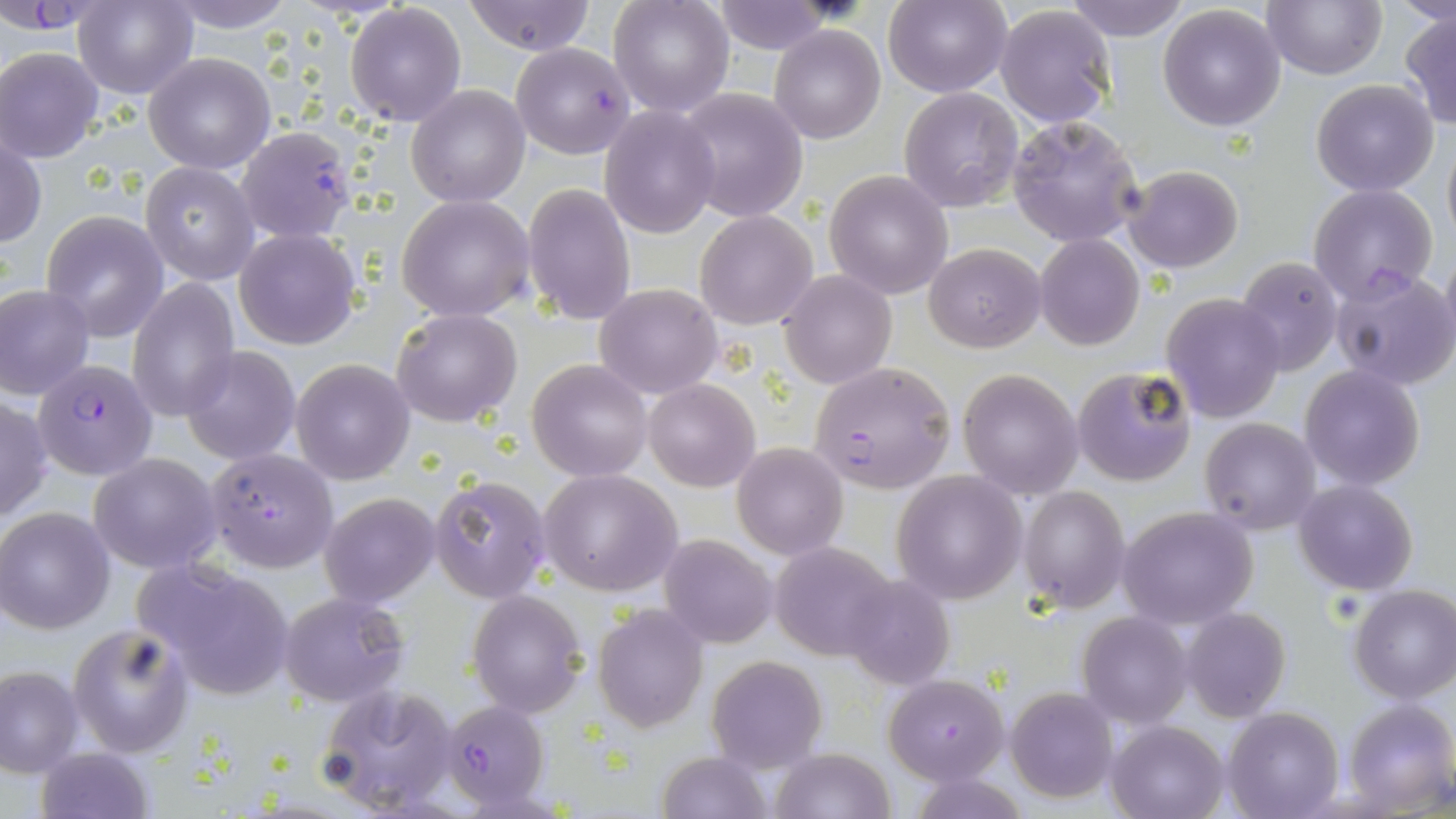

Approximate bounding boxes as [x1, y1, x2, y2] in pixels. Uninfected red blood cell locations: [165, 0, 293, 33], [462, 0, 597, 55], [607, 0, 734, 119], [884, 0, 1010, 97], [1063, 0, 1190, 42], [1263, 0, 1384, 80], [1392, 0, 1456, 31], [73, 1, 197, 101], [710, 2, 840, 53], [345, 3, 467, 127], [1157, 4, 1287, 131], [993, 5, 1116, 127], [1400, 11, 1456, 129], [770, 24, 887, 145], [0, 47, 104, 162], [143, 52, 276, 173], [1311, 79, 1440, 197], [406, 84, 530, 207], [898, 87, 1024, 213], [677, 88, 807, 221], [599, 105, 720, 238], [1008, 117, 1143, 247], [235, 126, 357, 242], [1, 136, 46, 249], [1442, 136, 1456, 248], [140, 162, 259, 283], [1123, 165, 1243, 273], [824, 169, 952, 299], [521, 182, 636, 326], [1309, 183, 1439, 302], [395, 193, 538, 322], [695, 210, 817, 330], [41, 212, 169, 340], [233, 227, 361, 350], [1034, 234, 1144, 351], [925, 242, 1046, 351], [1440, 244, 1456, 361], [1235, 256, 1343, 376], [1330, 265, 1455, 391], [778, 270, 896, 389], [128, 278, 240, 420], [595, 283, 724, 398], [0, 285, 95, 398], [1160, 293, 1286, 423], [392, 309, 521, 426], [181, 347, 301, 465], [527, 359, 653, 481], [291, 360, 414, 484], [1301, 365, 1424, 490], [1071, 366, 1198, 487], [958, 368, 1084, 498], [644, 378, 759, 490], [1, 392, 51, 525], [1201, 418, 1320, 535], [732, 441, 849, 560], [88, 452, 221, 575], [539, 468, 684, 596], [892, 468, 1026, 604], [432, 475, 550, 603], [1292, 479, 1418, 594], [1020, 485, 1131, 612], [319, 492, 440, 607], [1118, 506, 1260, 629], [1, 507, 116, 633], [661, 534, 779, 648], [769, 543, 894, 658], [131, 557, 298, 699], [842, 574, 958, 690], [1348, 585, 1456, 704], [468, 589, 588, 717], [279, 591, 408, 706], [593, 606, 709, 732], [1183, 609, 1292, 721], [1077, 612, 1192, 728], [68, 621, 197, 758], [706, 654, 828, 773], [0, 663, 82, 775], [884, 673, 1009, 784], [317, 685, 458, 815], [1005, 686, 1118, 803], [1346, 699, 1456, 811], [1223, 706, 1343, 819], [1107, 719, 1229, 819], [36, 746, 154, 819], [770, 748, 894, 819], [657, 750, 772, 819]. Plasmodium falciparum-infected red blood cell locations: [0, 5, 94, 35], [511, 42, 636, 158], [35, 359, 157, 480], [809, 361, 955, 493], [203, 448, 338, 572], [439, 700, 550, 810]. Slide-level diagnosis: Plasmodium falciparum. One field of a larger specimen. Image is 1456×819 pixels. Light microscopy. Thin blood film. May-Grünwald-Giemsa-stained preparation. Captured at 1000x magnification.